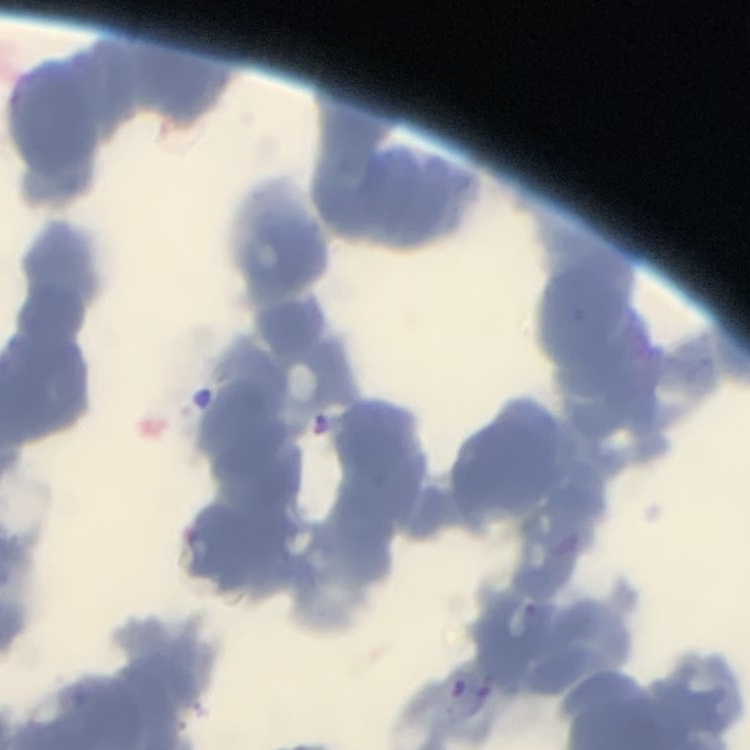
The erythrocytes exhibit rouleaux formation. Thin peripheral smear. Square crop of a larger photomicrograph. Stained with either Field's or Giemsa.